Assess this cell for malaria.
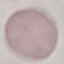

It is uninfected.

Photographed with a smartphone camera at the microscope eyepiece. Giemsa-stained preparation. Thin smear of blood. Cell patch, automatically extracted from a larger field of view and resized to 64 × 64 pixels.